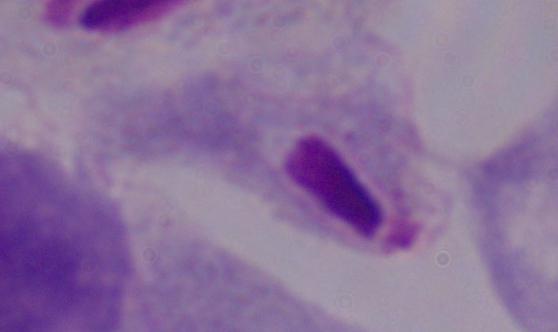
Summary:
  - Identification: trichomonad
  - Magnification: 1000x
  - Modality: photomicrograph